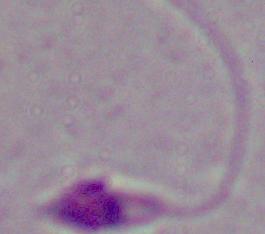
A Leishmania parasite is shown. Captured at 1000x magnification. Photomicrograph.